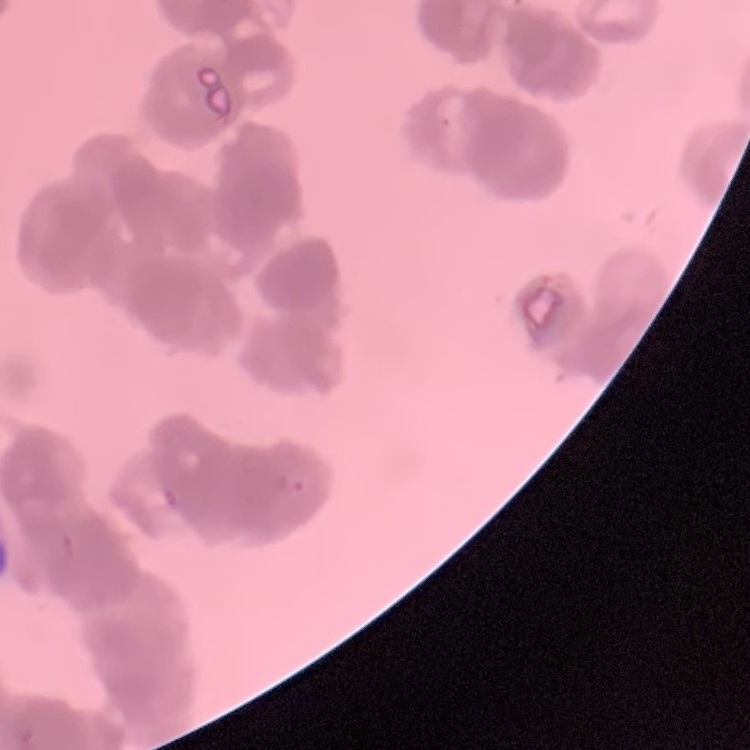

erythrocyte_morphology: rouleaux formation
stain: Field's or Giemsa
image_type: one tile cut from a larger photomicrograph
preparation: thin peripheral smear